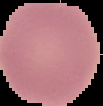

Summary:
  - Image size: 103×106 pixels
  - Preparation: thin blood smear
  - Result: negative for Plasmodium parasites
  - Image type: cell region segmented out of the field of view; surrounding area masked to black